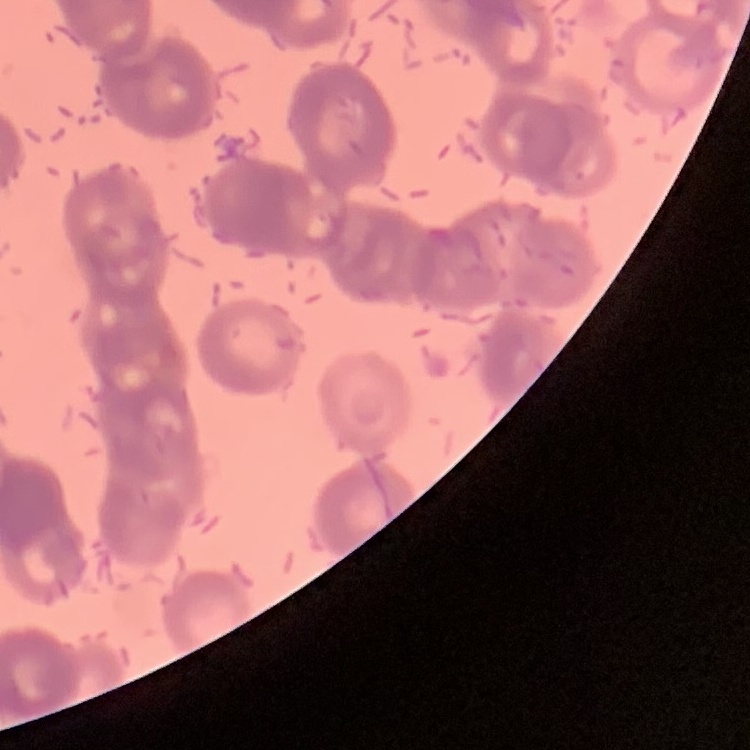
Summary:
  - Erythrocyte morphology: rouleaux formation
  - Image type: square crop of a larger photomicrograph
  - Preparation: thin blood film
  - Stain: Field's or Giemsa